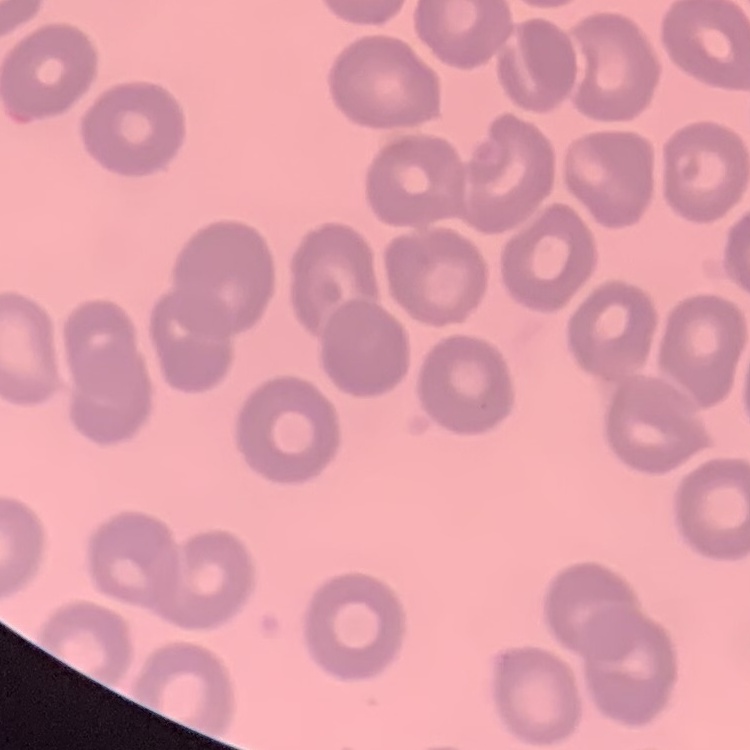 The red blood cells show no rouleaux formation. Square crop of a larger photomicrograph. Thin blood smear. Stained with either Field's or Giemsa.